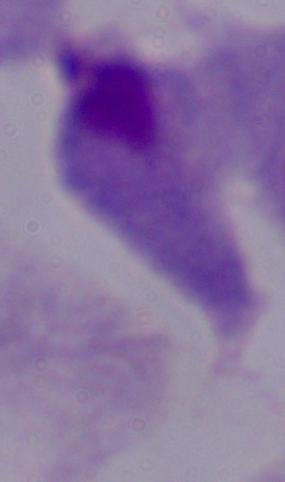
Summary:
  - Modality: photomicrograph
  - Magnification: 1000x
  - Identification: trichomonad